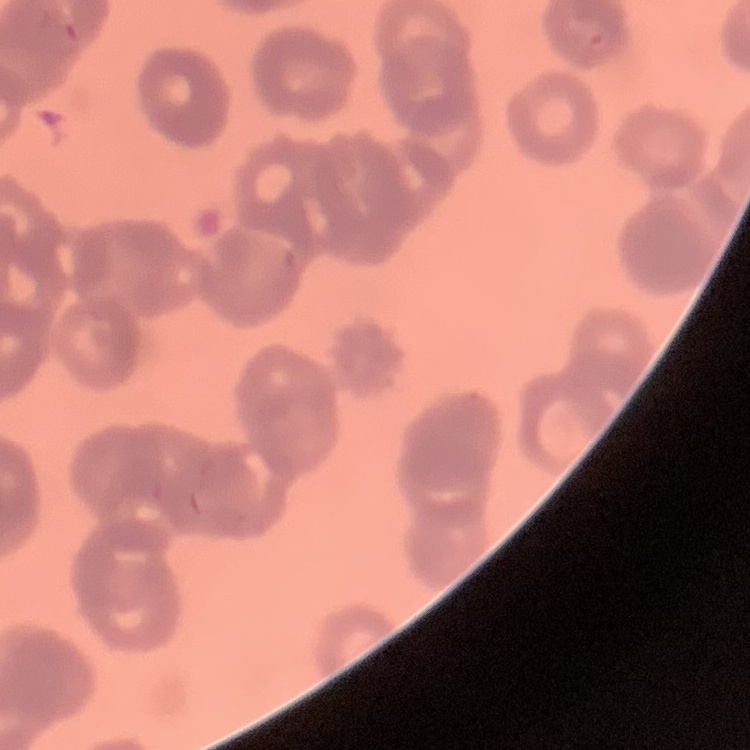
Summary:
  - Erythrocyte morphology: rouleaux formation
  - Image type: square crop of a larger photomicrograph
  - Preparation: thin blood film
  - Stain: Field's or Giemsa